Assess this cell for malaria.
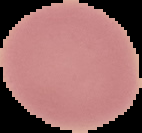

It is uninfected.

{
  "image_size": "142×133 pixels",
  "preparation": "thin blood film",
  "image_type": "cell region segmented out of the field of view; surrounding area masked to black"
}